Locate every Plasmodium parasite and every leukocyte.
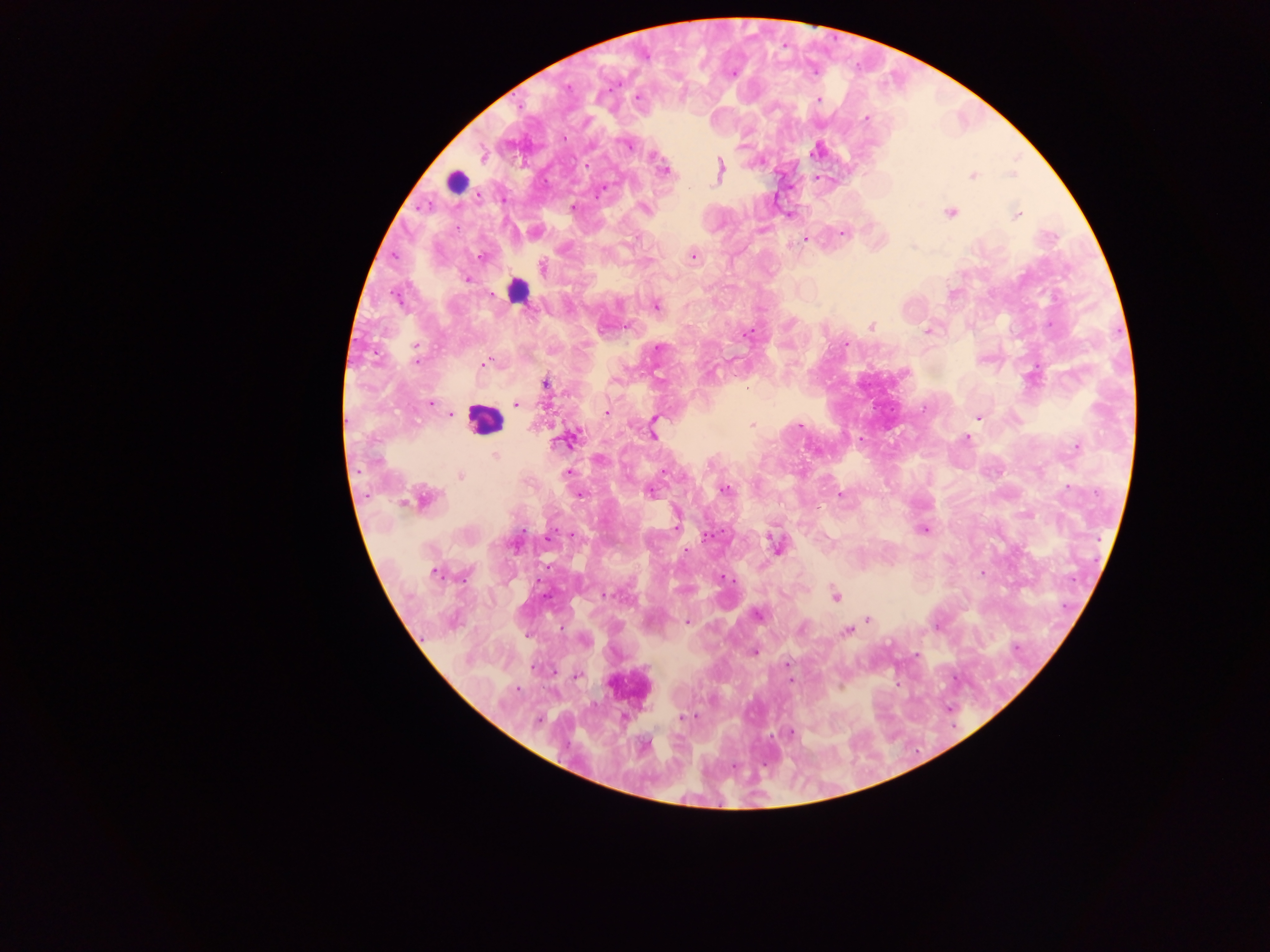

Approximate centers as x y in pixels.
Plasmodium parasites: 733 74; 637 98; 817 101; 864 118; 568 136; 628 144; 813 150; 665 170; 973 177; 597 192; 573 208; 644 208; 948 212; 1017 215; 762 230; 844 233; 803 240; 794 243; 912 247; 693 256; 482 257; 466 281; 656 305; 793 323; 870 326; 925 330; 745 332; 846 346; 658 349; 417 362; 483 365; 1039 366; 479 368; 712 370; 432 402; 516 405; 606 412; 449 415; 978 416; 535 424; 751 424; 799 426; 860 437; 966 438; 1074 446; 495 456; 568 472; 802 473; 461 475; 1069 487; 725 489; 651 493; 1096 493; 581 495; 840 497; 677 518; 923 530; 573 535; 708 535; 1100 542; 687 551; 1095 561; 435 573; 465 575; 720 577; 980 577; 1073 578; 541 582; 604 596; 756 615; 868 620; 686 622; 846 630; 754 654; 787 663; 576 678; 789 680; 518 686; 899 686; 841 688; 517 690; 681 717; 952 728.
Leukocytes: 455 182; 518 289; 485 415.

Collected in Ghana. Image is 1270×952 pixels. One field of view. Thick blood smear. Photographed through a microscope with a mobile-phone camera.